Assess this cell for malaria.
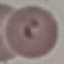
It is parasitized.

preparation = thin blood film
capture = smartphone camera at the microscope eyepiece
stain = Giemsa
image type = automatically extracted cell patch, resized to 64 × 64 pixels